Mark where platelets are.
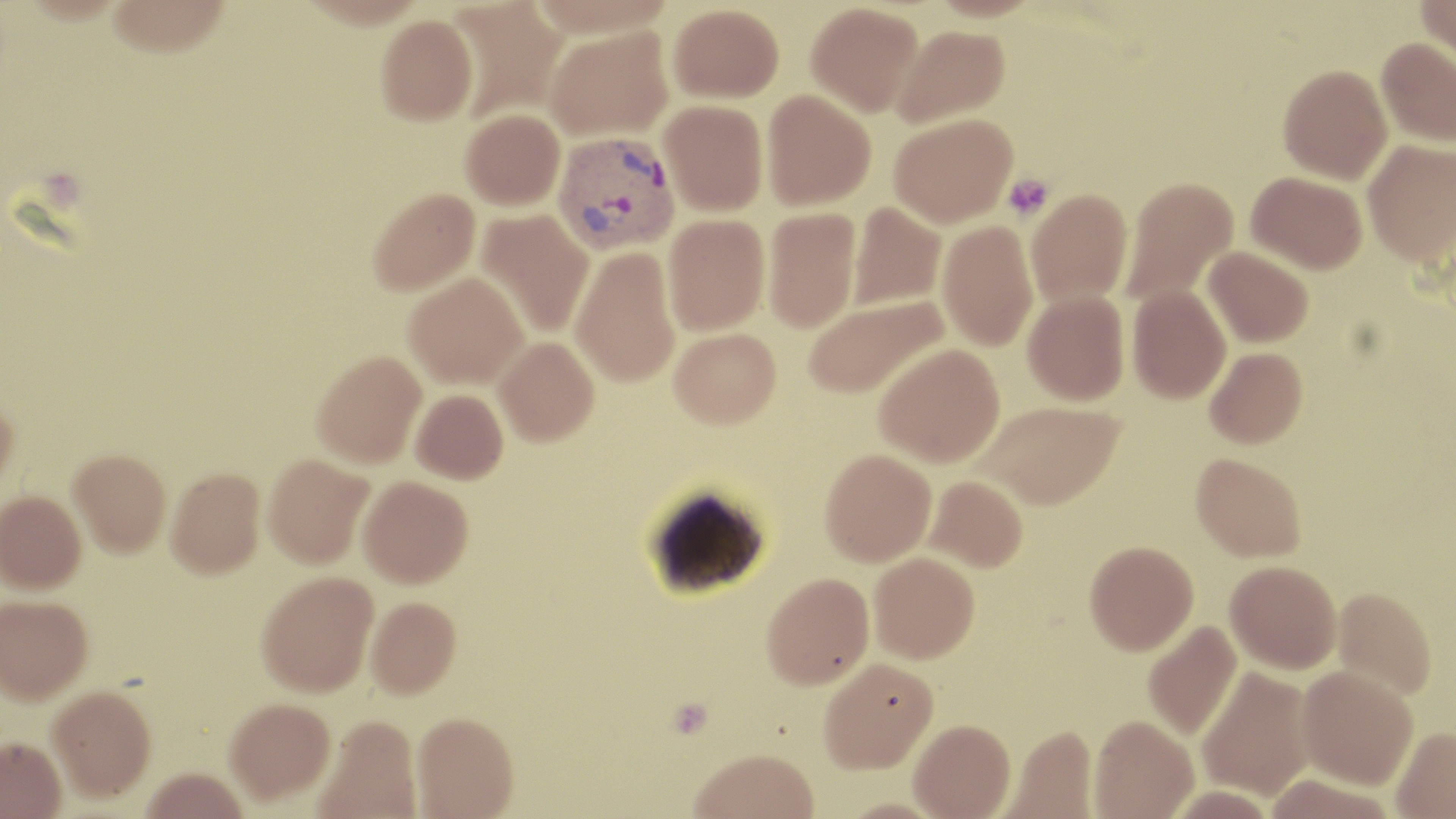

Approximate bounding boxes as named x1/y1/x2/y2 corners in pixels.
Platelets: (x1=1002, y1=174, x2=1055, y2=220).

Plasmodium vivax-infected red blood cell locations: (x1=553, y1=132, x2=681, y2=256). Uninfected red blood cell locations: (x1=106, y1=0, x2=233, y2=58), (x1=446, y1=0, x2=569, y2=120), (x1=1416, y1=0, x2=1456, y2=68), (x1=805, y1=2, x2=923, y2=116), (x1=668, y1=3, x2=784, y2=103), (x1=375, y1=15, x2=478, y2=125), (x1=891, y1=25, x2=1010, y2=127), (x1=543, y1=26, x2=674, y2=141), (x1=1376, y1=36, x2=1456, y2=147), (x1=1277, y1=64, x2=1393, y2=184), (x1=761, y1=90, x2=876, y2=210), (x1=659, y1=99, x2=768, y2=216), (x1=460, y1=109, x2=566, y2=210), (x1=888, y1=114, x2=1017, y2=228), (x1=1362, y1=139, x2=1456, y2=267), (x1=1246, y1=171, x2=1367, y2=273), (x1=1120, y1=176, x2=1239, y2=307), (x1=367, y1=188, x2=481, y2=296), (x1=1026, y1=189, x2=1133, y2=308), (x1=848, y1=202, x2=947, y2=310), (x1=762, y1=206, x2=862, y2=333), (x1=475, y1=208, x2=595, y2=339), (x1=663, y1=213, x2=770, y2=336), (x1=937, y1=221, x2=1039, y2=351), (x1=570, y1=245, x2=680, y2=388), (x1=1203, y1=246, x2=1313, y2=348), (x1=403, y1=271, x2=529, y2=389), (x1=1127, y1=285, x2=1231, y2=404), (x1=1023, y1=290, x2=1130, y2=406), (x1=801, y1=295, x2=949, y2=401), (x1=669, y1=327, x2=781, y2=428), (x1=493, y1=336, x2=599, y2=446), (x1=874, y1=342, x2=1006, y2=468), (x1=1204, y1=347, x2=1307, y2=448), (x1=312, y1=350, x2=426, y2=469), (x1=410, y1=389, x2=509, y2=485), (x1=0, y1=398, x2=19, y2=499), (x1=977, y1=401, x2=1124, y2=509), (x1=819, y1=448, x2=937, y2=567), (x1=68, y1=450, x2=171, y2=558), (x1=1191, y1=452, x2=1306, y2=561), (x1=263, y1=454, x2=374, y2=570), (x1=166, y1=468, x2=265, y2=581), (x1=924, y1=475, x2=1028, y2=572), (x1=358, y1=477, x2=473, y2=590), (x1=0, y1=491, x2=86, y2=594), (x1=1084, y1=541, x2=1198, y2=655), (x1=868, y1=552, x2=979, y2=664), (x1=1225, y1=560, x2=1341, y2=673), (x1=761, y1=572, x2=874, y2=690), (x1=256, y1=574, x2=378, y2=700), (x1=1332, y1=587, x2=1437, y2=700), (x1=0, y1=596, x2=93, y2=707), (x1=366, y1=598, x2=461, y2=701), (x1=1143, y1=619, x2=1242, y2=741), (x1=818, y1=657, x2=938, y2=774), (x1=1196, y1=665, x2=1316, y2=800), (x1=1297, y1=665, x2=1418, y2=789), (x1=48, y1=688, x2=156, y2=804), (x1=225, y1=701, x2=336, y2=809), (x1=411, y1=714, x2=519, y2=819), (x1=1089, y1=715, x2=1198, y2=818), (x1=314, y1=717, x2=422, y2=819), (x1=909, y1=719, x2=1015, y2=819), (x1=1001, y1=723, x2=1097, y2=818), (x1=1391, y1=727, x2=1456, y2=819), (x1=0, y1=739, x2=66, y2=819), (x1=688, y1=749, x2=820, y2=819), (x1=140, y1=772, x2=251, y2=819), (x1=1262, y1=774, x2=1398, y2=819). Slide-level diagnosis: Plasmodium vivax. May-Grünwald-Giemsa stain. Thin blood smear. 1000x magnification. One field of a larger specimen. Optical microscopy. Image is 1456×819 pixels.